Report the malaria status of this cell.
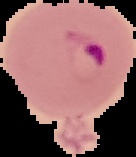

Parasitized.

image size = 136×157 pixels
preparation = thin blood smear
image type = segmented cell region with the area outside set to black